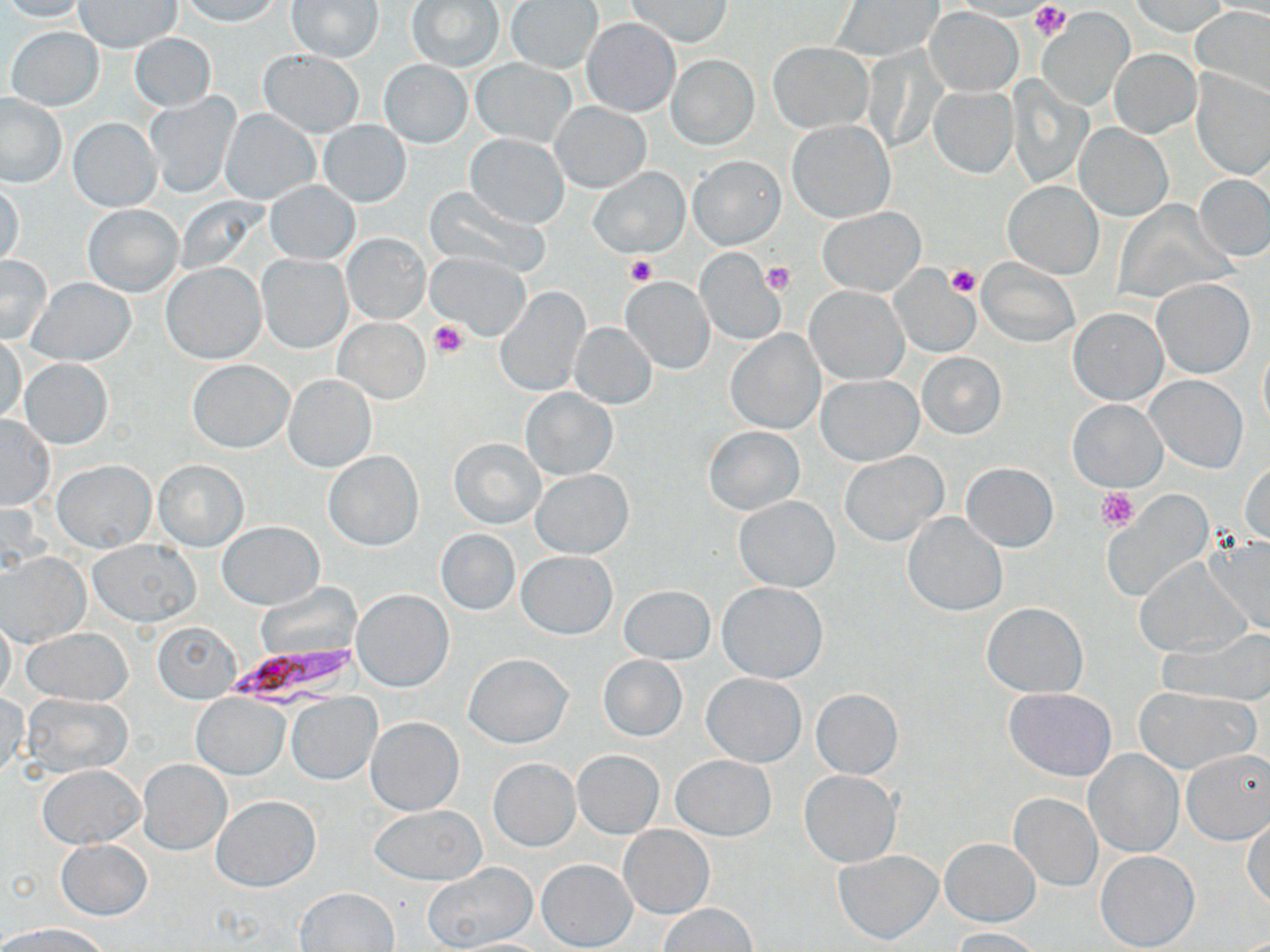

Summary:
  - Coordinate format: approximate bounding boxes as [x1, y1, x2, y2] in pixels
  - Platelet locations: [1028, 1, 1072, 40], [626, 255, 656, 286], [762, 261, 796, 295], [947, 264, 981, 298], [429, 320, 467, 359], [1098, 487, 1138, 530]
  - Plasmodium falciparum-infected red blood cell locations: [226, 643, 364, 712]
  - Uninfected red blood cell locations: [0, 0, 89, 22], [178, 0, 283, 26], [408, 0, 503, 70], [626, 0, 733, 47], [287, 1, 384, 62], [507, 1, 602, 72], [834, 1, 941, 61], [1131, 1, 1229, 36], [74, 2, 180, 52], [1191, 5, 1270, 98], [926, 7, 1022, 94], [1039, 11, 1131, 108], [581, 17, 680, 117], [6, 25, 105, 111], [129, 34, 217, 111], [768, 42, 871, 132], [257, 49, 365, 137], [1109, 50, 1200, 137], [666, 54, 759, 150], [471, 57, 578, 147], [379, 59, 472, 149], [1192, 70, 1270, 180], [1008, 81, 1093, 187], [930, 87, 1017, 177], [144, 92, 240, 197], [0, 93, 66, 187], [550, 102, 651, 193], [220, 110, 319, 204], [69, 118, 161, 212], [788, 119, 894, 223], [319, 120, 411, 206], [1074, 123, 1172, 222], [466, 134, 568, 228], [689, 155, 785, 249], [589, 167, 689, 257], [1194, 174, 1270, 262], [1003, 180, 1104, 279], [265, 181, 359, 264], [1, 182, 24, 268], [425, 185, 552, 279], [83, 204, 183, 297], [818, 208, 926, 295], [343, 233, 429, 324], [696, 247, 784, 344], [426, 253, 532, 339], [256, 254, 352, 353], [0, 256, 53, 345], [978, 258, 1080, 347], [161, 263, 266, 364], [889, 267, 980, 358], [623, 276, 715, 375], [28, 277, 135, 365], [1151, 278, 1255, 379], [495, 286, 589, 395], [805, 286, 907, 385], [1068, 306, 1168, 406], [334, 318, 430, 405], [569, 322, 656, 408], [727, 330, 824, 433], [0, 333, 25, 425], [1258, 339, 1270, 432], [915, 351, 1007, 439], [19, 358, 114, 449], [188, 359, 294, 453], [282, 373, 375, 472], [816, 374, 922, 465], [1146, 374, 1248, 473], [520, 387, 618, 480], [1068, 399, 1168, 492], [0, 415, 55, 510], [703, 426, 804, 515], [449, 438, 545, 528], [324, 451, 423, 551], [840, 451, 948, 546], [53, 460, 156, 552], [154, 460, 248, 550], [961, 462, 1059, 552], [1241, 463, 1270, 546], [530, 467, 634, 559], [734, 494, 841, 592], [1110, 500, 1208, 598], [903, 512, 1008, 616], [218, 521, 325, 610], [436, 530, 519, 615], [1203, 532, 1270, 639], [88, 539, 200, 627], [517, 551, 618, 640], [2, 553, 89, 646], [1133, 559, 1250, 658], [716, 582, 828, 682], [619, 584, 715, 665], [353, 590, 453, 691], [984, 604, 1086, 699], [0, 613, 17, 702], [153, 623, 241, 703], [23, 627, 134, 705], [1167, 629, 1270, 705], [463, 653, 573, 748], [597, 655, 686, 741], [701, 674, 807, 768], [1134, 687, 1257, 775], [810, 688, 904, 780], [1005, 688, 1116, 781], [0, 692, 28, 782], [21, 693, 135, 777], [287, 693, 382, 785], [192, 694, 287, 779], [366, 716, 464, 816], [1181, 749, 1270, 845], [572, 750, 664, 837], [1086, 750, 1182, 857], [672, 755, 776, 841], [488, 757, 580, 851], [138, 759, 231, 855], [38, 764, 143, 848], [800, 771, 901, 868], [1010, 792, 1101, 890], [213, 796, 320, 891], [370, 806, 487, 885], [1243, 813, 1270, 907], [618, 825, 714, 919], [941, 837, 1039, 926], [57, 840, 152, 921], [833, 850, 943, 945], [1095, 850, 1200, 951], [537, 859, 637, 951], [423, 862, 537, 950], [295, 886, 400, 951], [659, 902, 756, 951], [4, 924, 109, 952], [948, 926, 1047, 951], [445, 937, 554, 951]
  - Slide-level diagnosis: Plasmodium falciparum
  - Magnification: 1000x
  - Image size: 1270×952 pixels
  - Preparation: thin blood smear
  - Modality: light microscopy
  - Stain: May-Grünwald-Giemsa
  - Field of view: single